Give the position of every Plasmodium parasite.
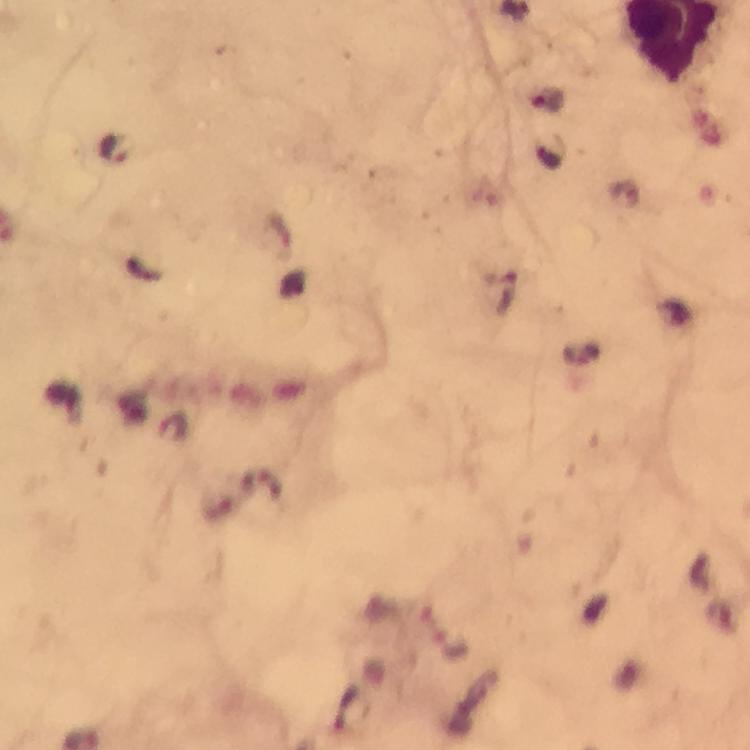

Approximate centers as [x, y] in pixels.
Plasmodium parasites: [114, 148].

Thick blood film. Giemsa stain. Image is 750×750 pixels. Smartphone photograph taken through a microscope. A crop from one field of view. Immersion oil was used. 100x magnification. From a malaria diagnostic workup.